Give the position of every Plasmodium parasite visible.
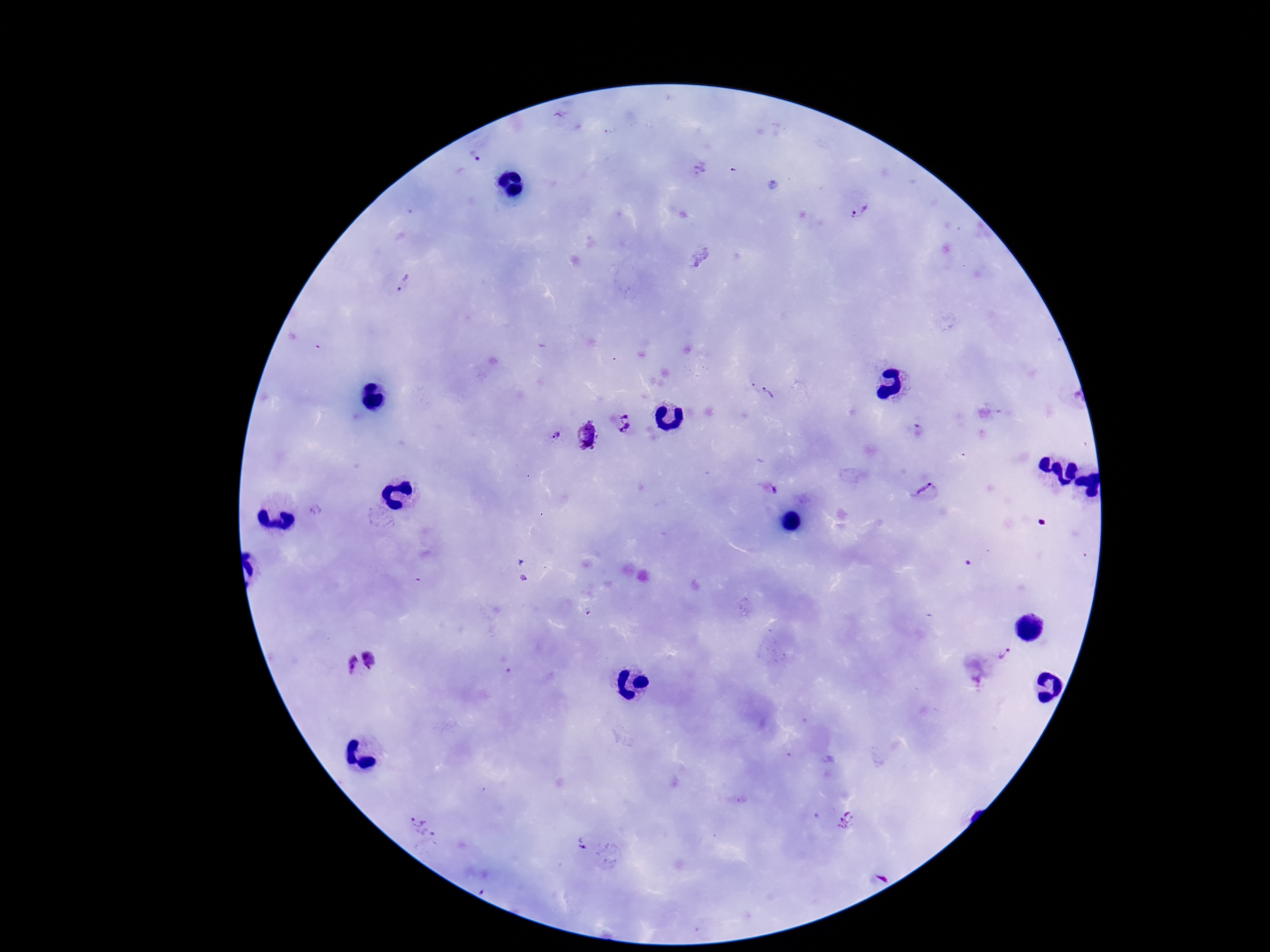
Approximate centers as (x, y) in pixels.
Plasmodium parasites: (558, 115), (735, 171), (860, 212), (404, 284), (762, 389), (623, 422), (586, 435), (556, 436), (774, 492), (928, 492), (524, 578), (1004, 654), (373, 657), (349, 664), (977, 671), (846, 820), (421, 827), (581, 843).

Summary:
  - Preparation: thick blood film
  - Stain: Giemsa
  - Image size: 1270×952 pixels
  - Field of view: one from this slide
  - Magnification: 100x
  - Patient malaria status: positive
  - Capture: smartphone camera through the microscope eyepiece